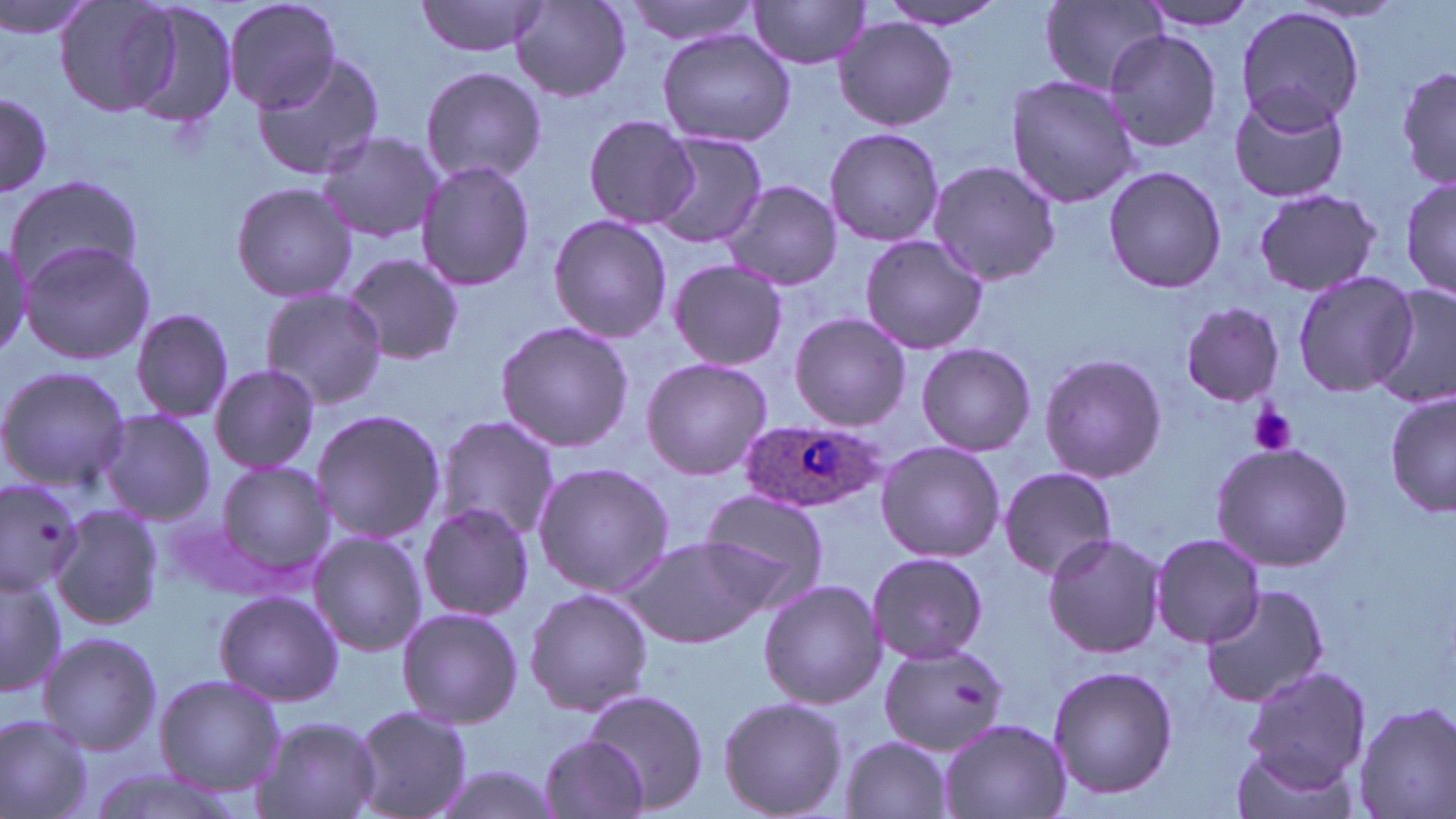

{
  "plasmodium_ovale_infected_red_blood_cell_locations": "approximate bounding boxes as [x1, y1, x2, y2] in pixels: [739, 418, 885, 514]",
  "slide_level_diagnosis": "Plasmodium ovale",
  "preparation": "thin blood film",
  "uninfected_red_blood_cell_locations": "approximate bounding boxes as [x1, y1, x2, y2] in pixels: [0, 0, 106, 42], [56, 0, 187, 115], [223, 0, 343, 112], [620, 0, 766, 46], [113, 1, 238, 131], [417, 1, 548, 57], [747, 1, 873, 69], [876, 1, 1009, 29], [1136, 1, 1264, 31], [1039, 2, 1169, 94], [512, 3, 633, 102], [1236, 5, 1365, 131], [833, 16, 958, 131], [656, 28, 796, 147], [1102, 29, 1224, 155], [250, 53, 385, 183], [1395, 63, 1454, 195], [420, 67, 549, 187], [1005, 74, 1141, 209], [1228, 91, 1351, 204], [0, 92, 52, 198], [583, 114, 699, 231], [824, 127, 946, 246], [316, 131, 442, 245], [651, 132, 769, 248], [928, 160, 1063, 285], [416, 161, 536, 291], [1101, 166, 1228, 294], [1398, 173, 1455, 302], [6, 176, 144, 290], [231, 181, 356, 303], [722, 182, 843, 291], [1251, 187, 1383, 299], [548, 213, 671, 344], [0, 233, 31, 358], [860, 234, 990, 353], [20, 240, 154, 365], [340, 253, 465, 364], [668, 258, 788, 371], [1291, 271, 1418, 396], [1371, 284, 1456, 408], [259, 286, 389, 409], [1181, 303, 1284, 406], [130, 310, 237, 424], [789, 314, 912, 430], [494, 320, 632, 453], [916, 343, 1035, 457], [1040, 351, 1167, 482], [640, 357, 772, 480], [208, 363, 321, 475], [0, 365, 129, 491], [1387, 391, 1455, 519], [96, 408, 216, 526], [311, 409, 446, 543], [434, 415, 559, 542], [1210, 439, 1355, 573], [874, 440, 1004, 563], [211, 461, 336, 582], [532, 461, 673, 599], [998, 467, 1118, 580], [0, 479, 87, 593], [694, 487, 831, 608], [417, 501, 535, 621], [49, 502, 161, 632], [1041, 530, 1167, 659], [308, 531, 427, 656], [622, 534, 774, 648], [1151, 534, 1265, 646], [867, 551, 989, 666], [0, 568, 65, 699], [757, 578, 884, 710], [1201, 581, 1330, 708], [524, 588, 654, 717], [212, 590, 342, 707], [396, 607, 523, 727], [35, 631, 161, 754], [877, 643, 1010, 756], [1046, 664, 1178, 800], [1241, 666, 1370, 788], [154, 673, 284, 796], [584, 689, 708, 812], [718, 696, 847, 818], [1352, 702, 1456, 819], [349, 704, 474, 819], [0, 713, 95, 819], [254, 715, 382, 819], [939, 718, 1069, 819], [536, 733, 650, 818], [840, 735, 954, 818], [1230, 743, 1356, 819], [425, 763, 564, 819], [84, 766, 244, 819]",
  "modality": "optical microscopy",
  "platelet_locations": "approximate bounding boxes as [x1, y1, x2, y2] in pixels: [1248, 403, 1299, 456]",
  "field_of_view": "one of a larger specimen",
  "magnification": "1000x",
  "image_size": "1456×819 pixels",
  "stain": "May-Grünwald-Giemsa"
}